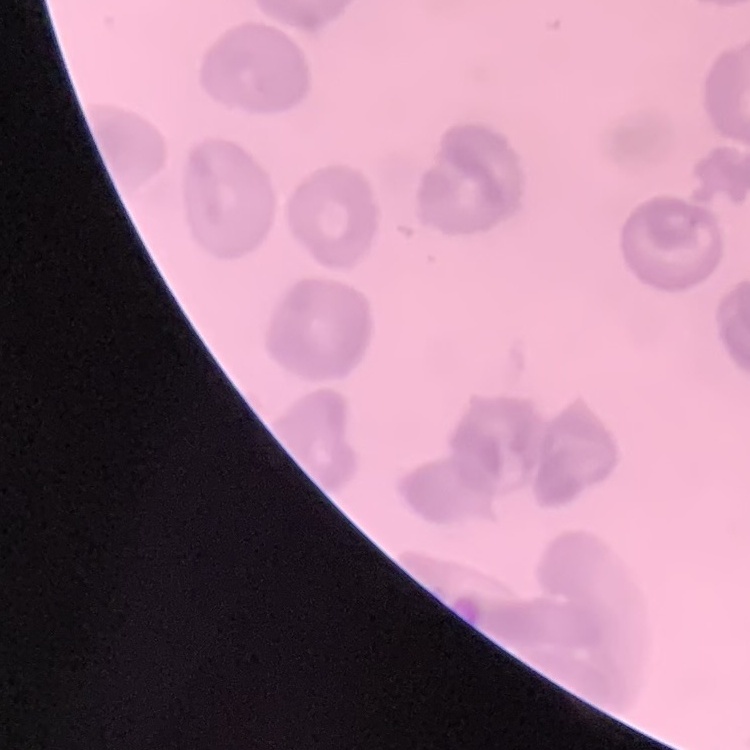 The erythrocytes show no rouleaux formation. Thin peripheral smear. One tile cut from a larger photomicrograph. Field's or Giemsa stain.